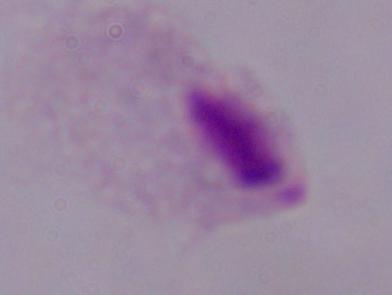
modality: photomicrograph
identification: trichomonad
magnification: 1000x